Name the parasite shown.
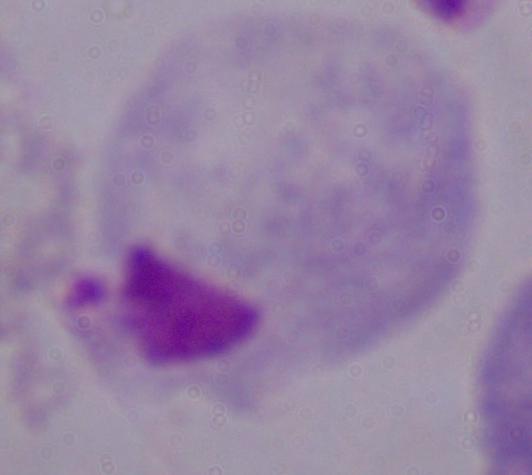

This is a trichomonad.

Photomicrograph. 1000x magnification.